Give the position of every Plasmodium parasite visible.
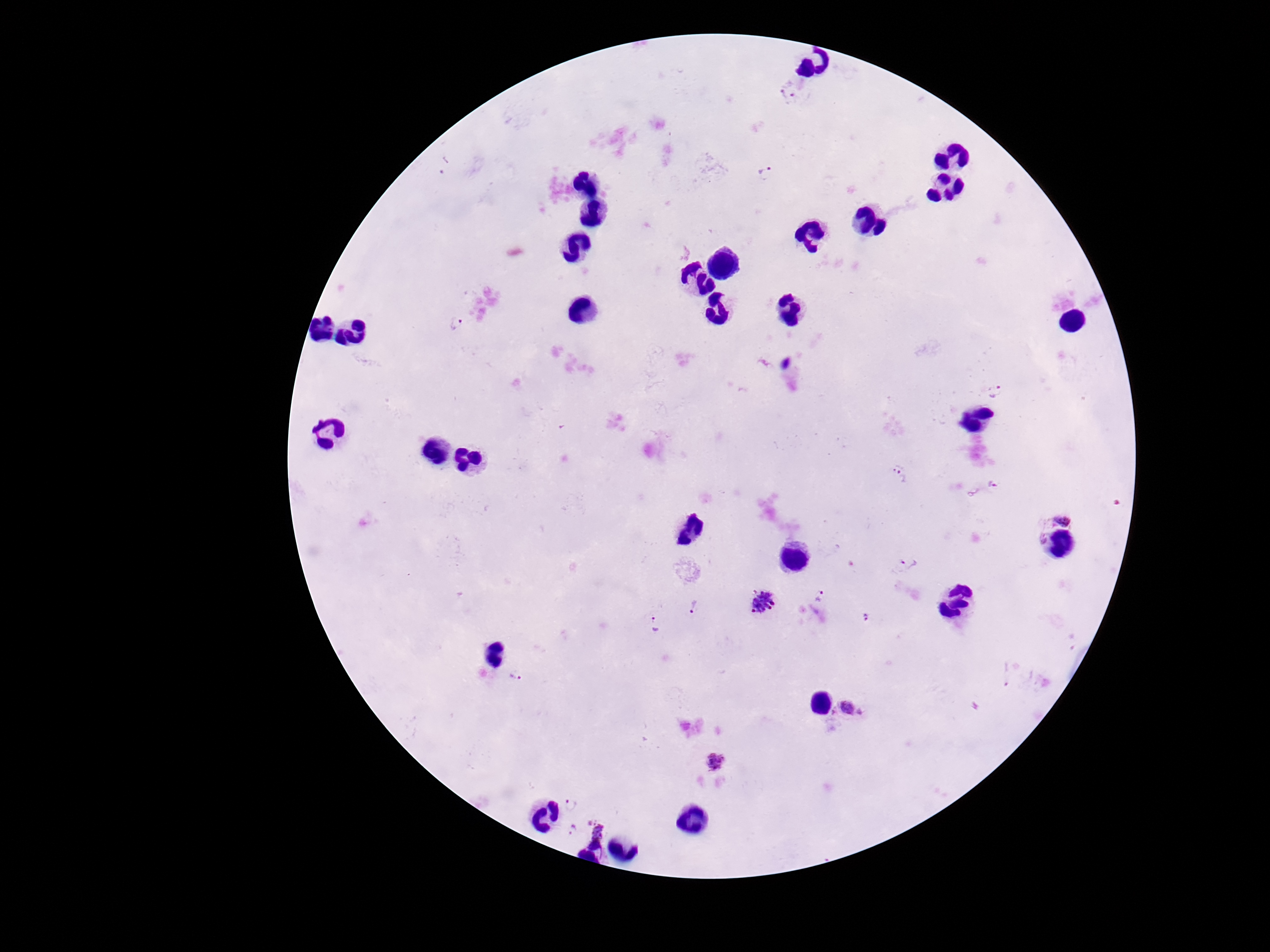

Approximate object centers, in pixels from the top-left corner.
Plasmodium parasites: (x=788, y=92), (x=765, y=173), (x=455, y=325), (x=995, y=390), (x=900, y=475), (x=993, y=486), (x=1061, y=519), (x=1037, y=537), (x=907, y=565), (x=819, y=596), (x=763, y=603), (x=693, y=607), (x=866, y=617), (x=657, y=625), (x=515, y=678), (x=1008, y=678), (x=849, y=710), (x=715, y=763), (x=570, y=805), (x=575, y=830), (x=600, y=830).

stain: Giemsa
magnification: 100x
capture: smartphone camera through the microscope eyepiece
preparation: thick blood smear
image_size: 1270×952 pixels
field_of_view: single
patient_malaria_status: infected